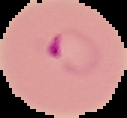
Summary:
  - Preparation: thin blood film
  - Malaria status: parasitized
  - Image size: 127×118 pixels
  - Image type: cell region segmented out of the field of view; surrounding area masked to black